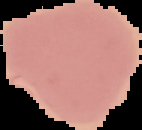
Summary:
  - Preparation: thin blood film
  - Image type: segmented cell region with the area outside set to black
  - Image size: 142×130 pixels
  - Malaria status: uninfected